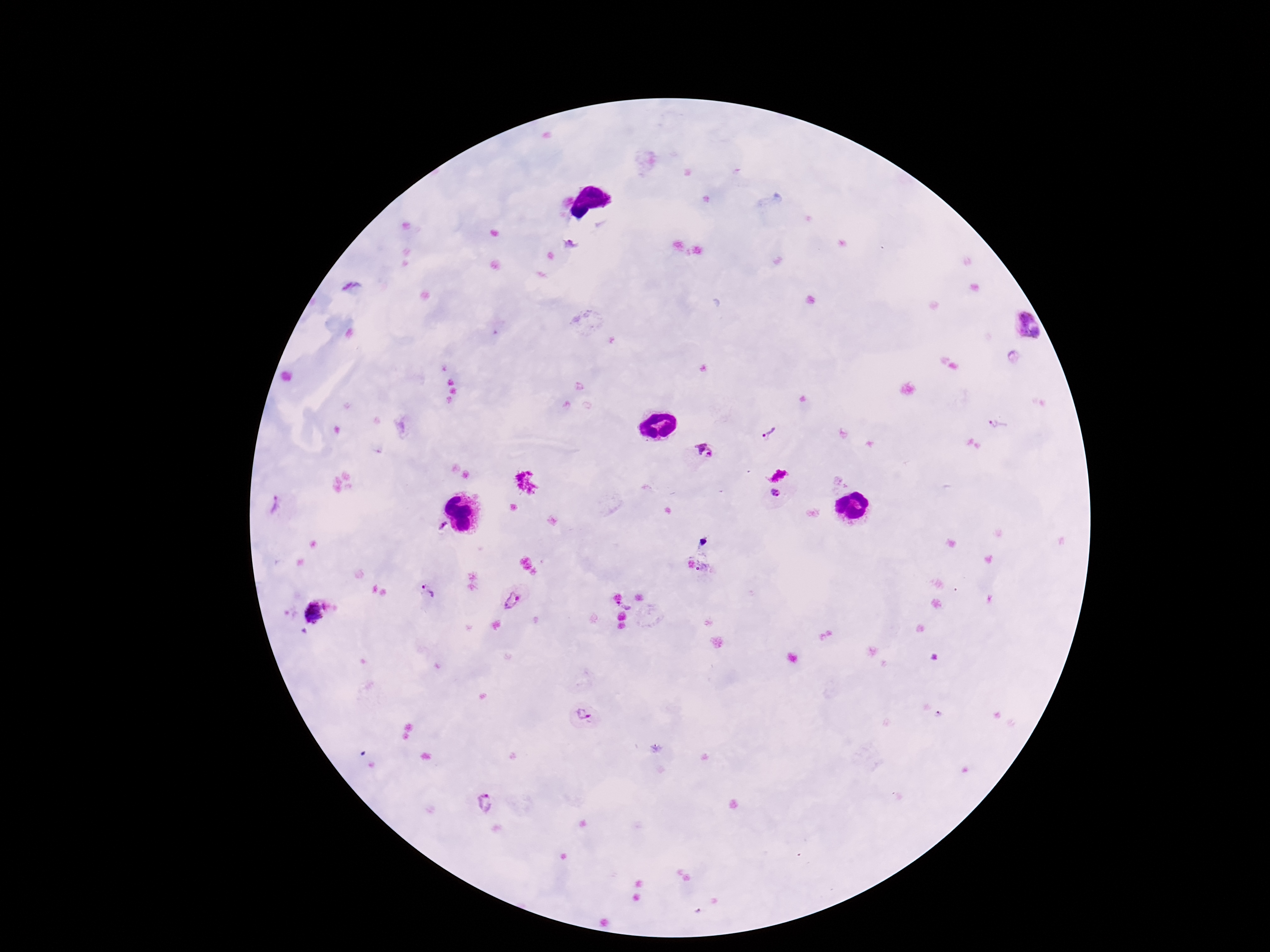
Approximate centers as [x, y] in pixels.
Summary:
  - Plasmodium parasite locations: [572, 244], [1025, 326], [998, 423], [769, 433], [704, 450], [779, 472], [778, 492], [274, 506], [443, 526], [428, 591], [512, 599], [626, 604], [316, 612], [593, 714], [486, 804]
  - Stain: Giemsa
  - Magnification: 100x
  - Patient malaria status: infected
  - Capture: smartphone camera through the microscope eyepiece
  - Preparation: thick peripheral-blood smear
  - Image size: 1270×952 pixels
  - Field of view: single